Assess this cell for malaria.
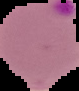
It is parasitized.

{
  "image_size": "79×91 pixels",
  "preparation": "thin blood smear",
  "image_type": "segmented cell region on a black background"
}